Identify the cell.
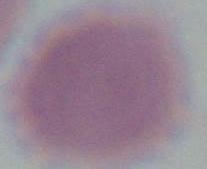
An erythrocyte.

Micrograph. 1000x magnification.